Assess for Plasmodium parasites.
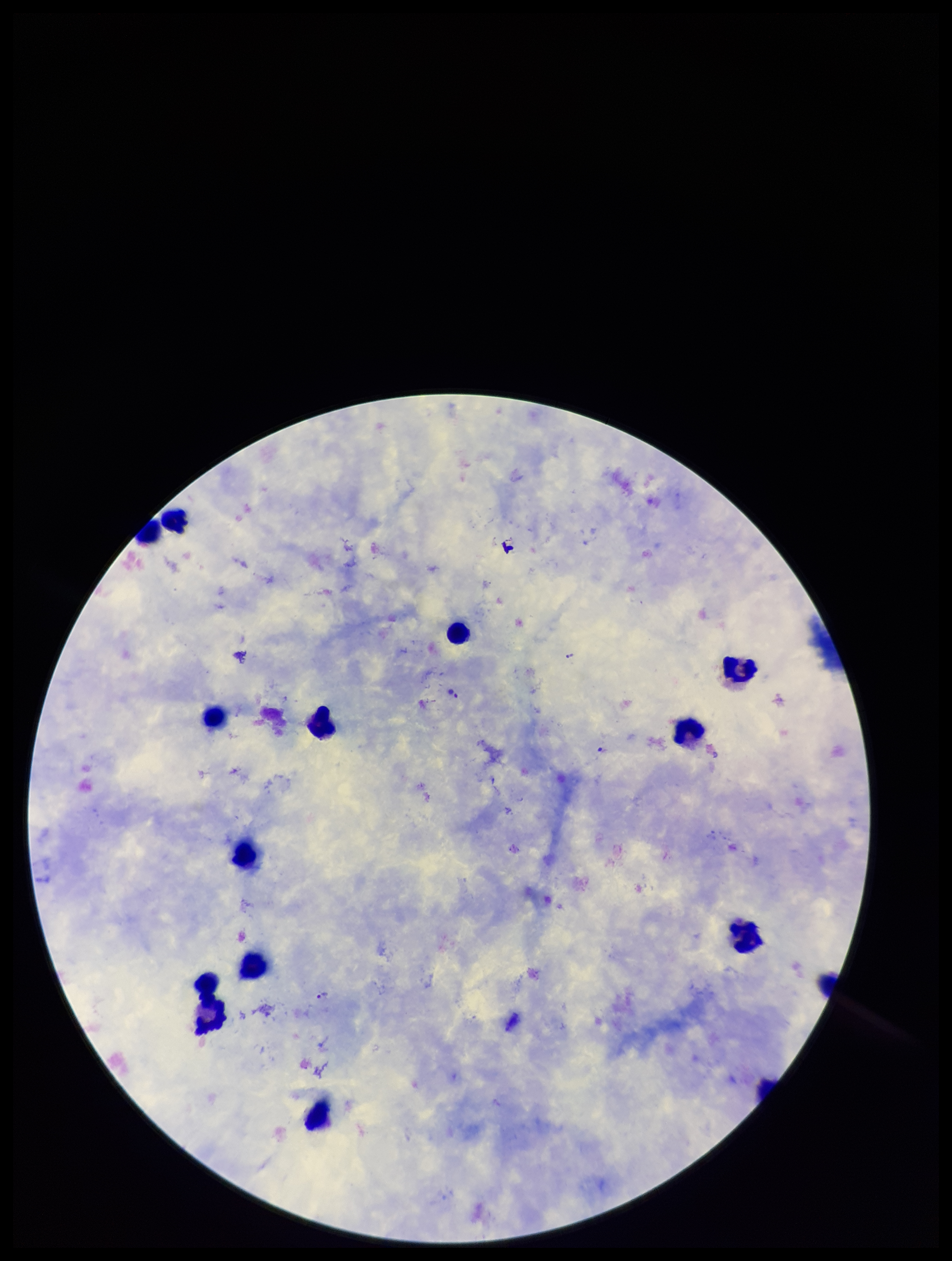

Seen.

capture = smartphone photograph through the microscope eyepiece
species reported for this patient = Plasmodium falciparum
image size = 952×1261 pixels
field of view = single
stain = Giemsa
parasite count = 4
preparation = thick
leukocyte count = 12
patient malaria status = positive